Report the malaria status of this cell.
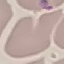
It is uninfected.

Giemsa-stained preparation. Automatically extracted cell patch, resized to 64 × 64 pixels. Photographed with a smartphone camera at the microscope eyepiece. Thin smear of blood.